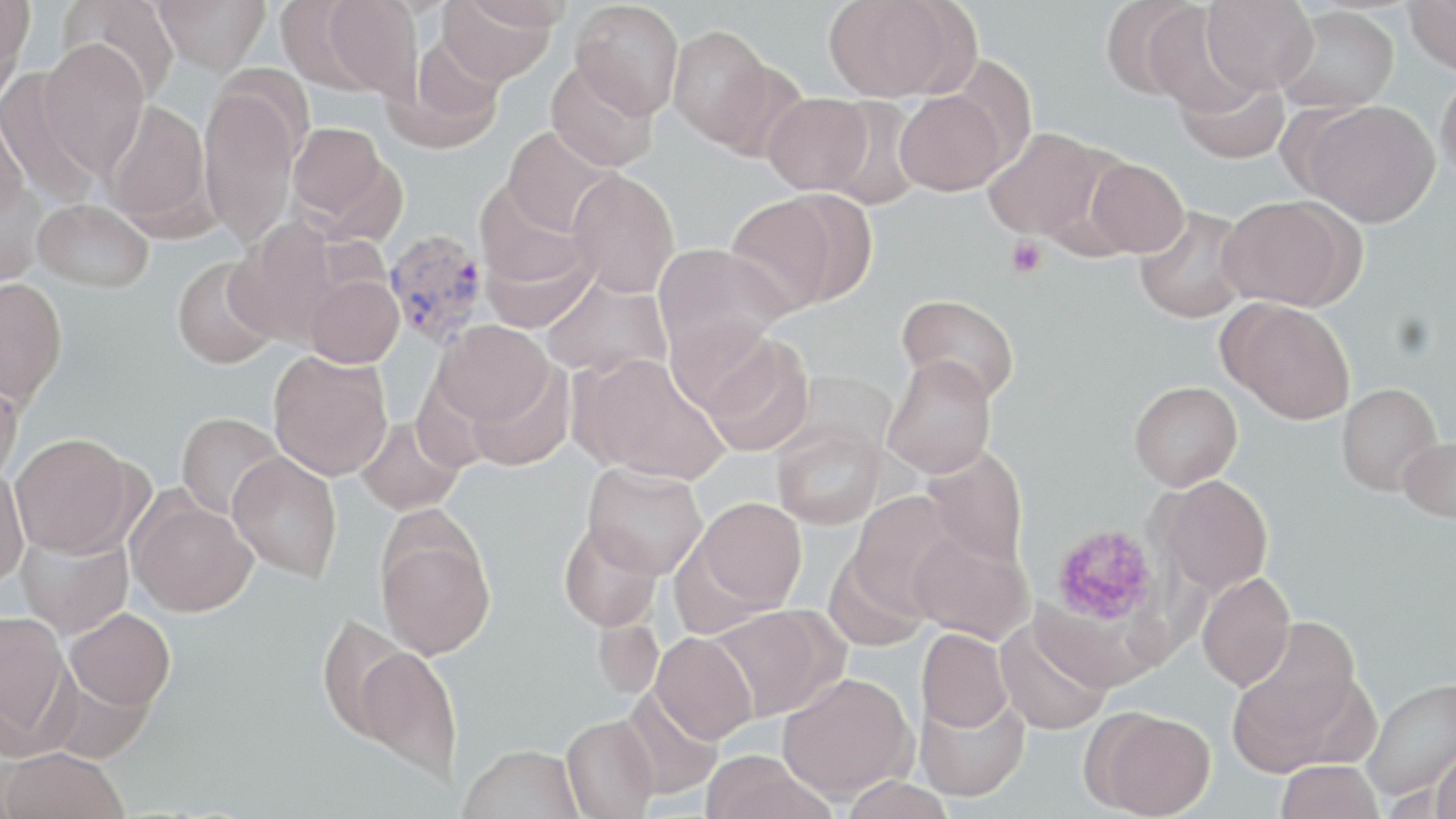
slide-level diagnosis = Plasmodium vivax
uninfected red blood cell locations = approximate bounding boxes as (x1, y1, x2, y2) in pixels: (1, 0, 35, 82), (58, 0, 181, 102), (153, 0, 271, 75), (318, 0, 422, 98), (436, 0, 557, 86), (449, 0, 576, 32), (823, 0, 967, 101), (1099, 0, 1209, 100), (1201, 0, 1317, 95), (1404, 0, 1456, 74), (570, 1, 685, 118), (1141, 5, 1252, 115), (1276, 5, 1399, 114), (668, 25, 774, 147), (386, 38, 508, 154), (38, 40, 150, 173), (546, 59, 658, 171), (707, 59, 809, 164), (1436, 68, 1456, 186), (0, 69, 106, 207), (1173, 72, 1291, 163), (199, 85, 301, 245), (896, 89, 1008, 195), (762, 92, 874, 196), (821, 96, 928, 209), (104, 99, 213, 234), (1300, 99, 1441, 227), (0, 108, 30, 225), (286, 122, 391, 224), (502, 127, 616, 236), (983, 127, 1113, 242), (1083, 156, 1189, 258), (566, 169, 680, 297), (0, 179, 48, 287), (725, 193, 841, 315), (1218, 195, 1360, 310), (33, 198, 153, 292), (1134, 206, 1252, 324), (225, 220, 344, 347), (479, 233, 596, 333), (653, 243, 789, 359), (172, 256, 280, 369), (304, 274, 404, 367), (540, 276, 673, 380), (0, 278, 68, 407), (896, 293, 1021, 403), (1222, 299, 1356, 424), (666, 314, 779, 417), (434, 321, 554, 426), (698, 333, 815, 456), (268, 351, 393, 481), (571, 352, 731, 482), (882, 356, 997, 478), (464, 364, 576, 472), (0, 369, 24, 485), (785, 371, 898, 462), (1129, 380, 1243, 490), (1336, 382, 1442, 495), (176, 411, 284, 520), (355, 415, 464, 516), (772, 425, 886, 529), (9, 432, 142, 558), (1397, 437, 1456, 522), (921, 445, 1028, 565), (228, 452, 342, 581), (582, 461, 707, 578), (0, 465, 28, 590), (1156, 474, 1274, 596), (847, 491, 961, 615), (127, 493, 257, 618), (693, 497, 807, 613), (558, 520, 663, 632), (377, 527, 495, 660), (15, 529, 133, 640), (908, 530, 1034, 644), (822, 548, 931, 653), (1197, 572, 1296, 691), (708, 604, 842, 721), (63, 608, 175, 712), (1, 610, 73, 753), (314, 613, 418, 745), (593, 617, 664, 700), (995, 617, 1112, 736), (1229, 620, 1364, 764), (917, 628, 1013, 732), (651, 632, 757, 743), (354, 645, 463, 784), (777, 672, 916, 803), (1361, 676, 1456, 799), (618, 687, 724, 802), (915, 692, 1029, 803), (1087, 708, 1217, 818), (561, 715, 659, 819), (460, 744, 584, 819), (1431, 744, 1456, 819), (1, 747, 128, 819), (699, 750, 835, 819), (1275, 760, 1382, 819), (840, 776, 955, 819)
platelet locations = approximate bounding boxes as (x1, y1, x2, y2) in pixels: (1005, 237, 1047, 277), (1049, 523, 1162, 628)
image size = 1456×819 pixels
preparation = thin blood film
field of view = single
magnification = 1000x
Plasmodium vivax-infected red blood cell locations = approximate bounding boxes as (x1, y1, x2, y2) in pixels: (381, 227, 489, 349)
modality = light microscopy
stain = May-Grünwald-Giemsa